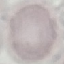
Result: negative for malaria parasites. Acquired by smartphone through the microscope eyepiece. Thin blood film. Cell patch, automatically extracted from a larger field of view and resized to 64 × 64 pixels. Giemsa stain.